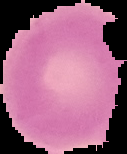

Cell region segmented out of the field of view; the surrounding area is masked to black. Image is 127×154 pixels. Result: no malaria parasites detected. From a thin blood smear.